Name the parasite shown.
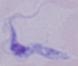
A trypanosome.

Summary:
  - Magnification: 1000x
  - Modality: micrograph